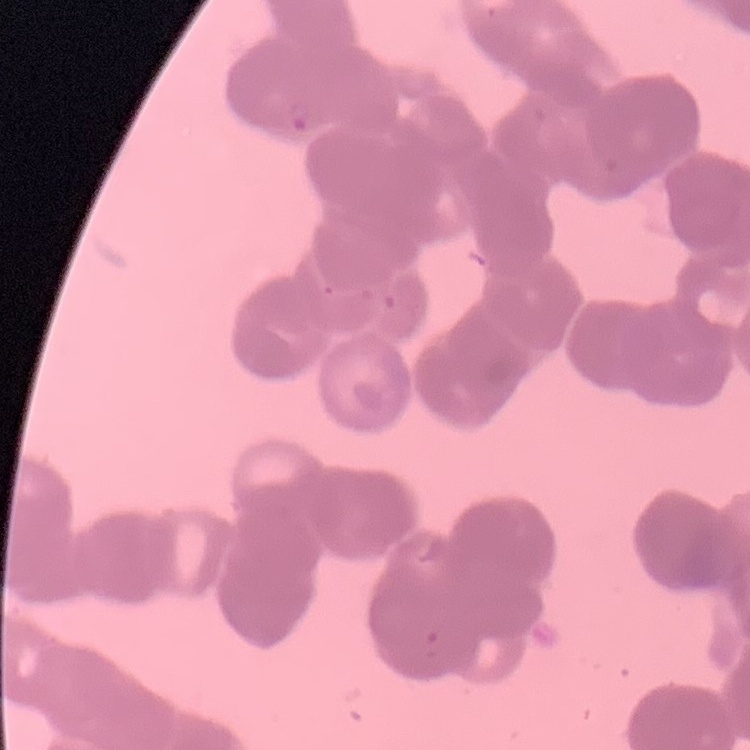
Summary:
  - Red blood cell morphology: rouleaux formation
  - Preparation: thin peripheral smear
  - Stain: Field's or Giemsa
  - Image type: square crop of a larger photomicrograph